State which parasite is depicted.
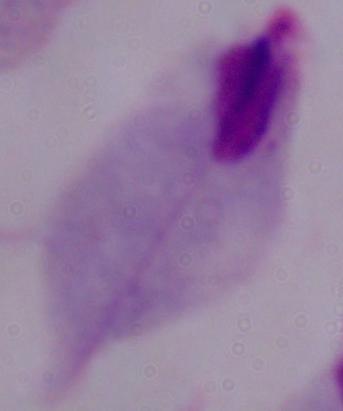

A trichomonad.

Photomicrograph. 1000x magnification.